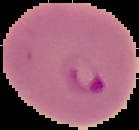
Summary:
  - Image type: cell region segmented out of the field of view; surrounding area masked to black
  - Malaria status: parasitized
  - Image size: 139×130 pixels
  - Preparation: thin blood film